State the blood parasite species.
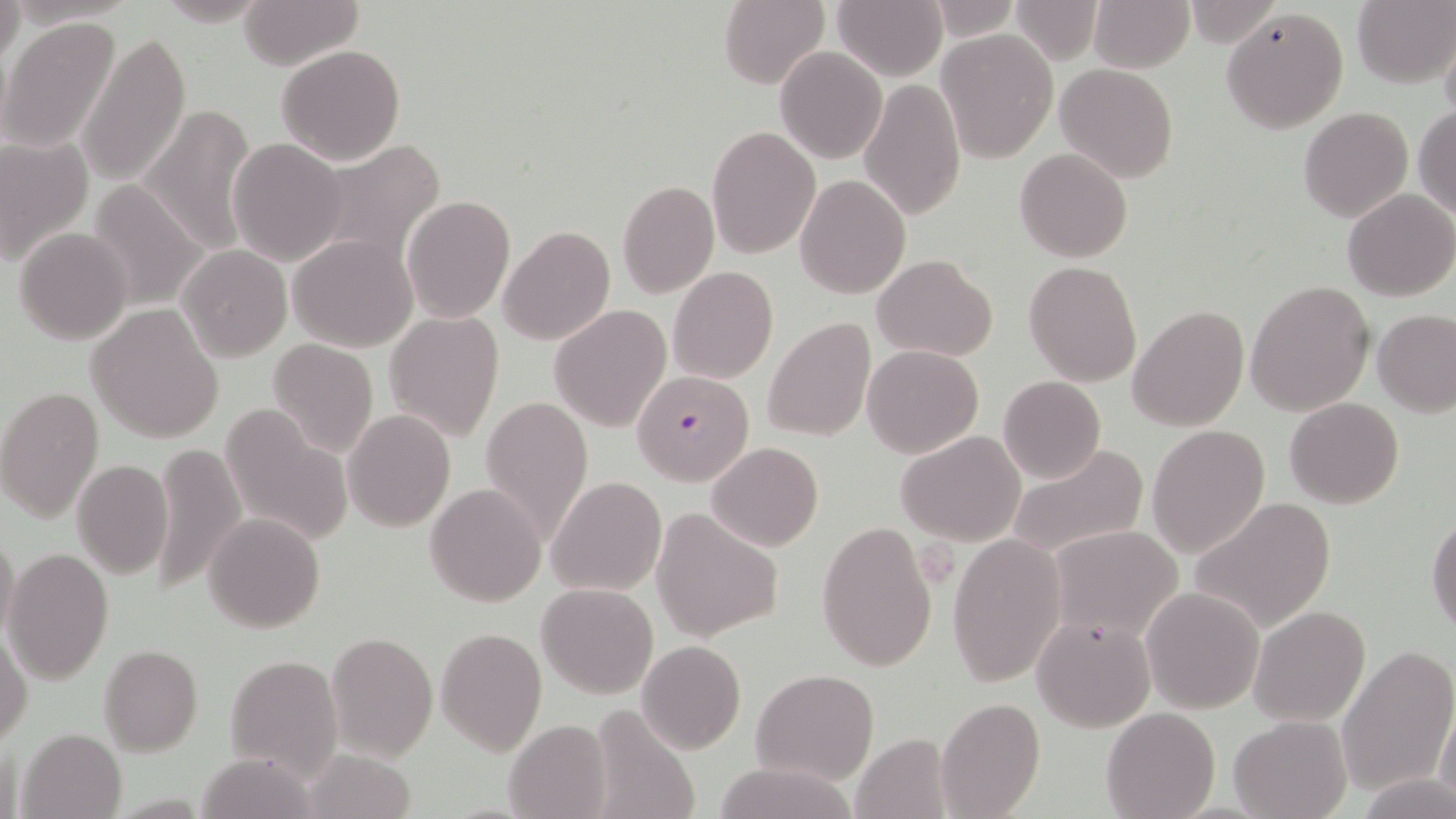

Plasmodium falciparum.

Summary:
  - Coordinate format: approximate bounding boxes as (x1,y1)-(x2,y2) corner pairs in pixels
  - Plasmodium falciparum-infected red blood cell locations: (632,369)-(755,486)
  - Uninfected red blood cell locations: (0,0)-(25,69), (150,0)-(274,27), (237,0)-(363,69), (720,0)-(830,89), (830,0)-(946,79), (1011,0)-(1104,63), (1088,0)-(1194,72), (1353,2)-(1454,87), (1220,7)-(1348,133), (2,17)-(123,154), (1441,27)-(1456,125), (937,30)-(1057,161), (79,33)-(190,186), (276,44)-(406,165), (774,47)-(886,163), (1056,63)-(1178,181), (861,76)-(966,221), (139,102)-(256,256), (1412,106)-(1456,219), (1298,107)-(1413,222), (707,126)-(820,258), (0,133)-(94,267), (227,137)-(347,266), (310,140)-(443,275), (1014,148)-(1134,263), (795,174)-(910,298), (617,179)-(719,298), (86,180)-(209,310), (1343,188)-(1456,302), (403,195)-(515,323), (498,226)-(615,346), (13,227)-(134,344), (288,235)-(419,352), (178,245)-(291,361), (873,254)-(998,361), (1024,261)-(1143,386), (668,265)-(778,383), (1245,279)-(1374,416), (86,303)-(226,443), (1128,304)-(1251,432), (550,306)-(671,431), (1373,308)-(1455,416), (384,310)-(505,442), (760,317)-(876,443), (267,338)-(379,460), (863,345)-(983,458), (998,376)-(1106,484), (0,385)-(104,524), (481,395)-(593,545), (1284,397)-(1405,508), (218,402)-(353,550), (342,408)-(455,532), (1146,424)-(1271,558), (897,430)-(1025,545), (151,441)-(247,597), (706,442)-(823,552), (1008,444)-(1148,561), (71,459)-(173,580), (547,475)-(667,596), (426,482)-(546,606), (1189,496)-(1337,634), (203,511)-(325,632), (650,511)-(783,640), (1427,513)-(1456,635), (815,520)-(938,673), (1049,524)-(1185,642), (0,527)-(20,645), (947,533)-(1066,687), (4,547)-(114,682), (537,581)-(657,699), (1140,586)-(1266,715), (1248,605)-(1373,726), (1033,615)-(1155,733), (436,626)-(547,756), (1,629)-(32,747), (325,632)-(439,762), (636,639)-(747,754), (1335,644)-(1455,797), (98,645)-(203,756), (223,653)-(342,779), (753,668)-(877,786), (937,697)-(1044,818), (1434,697)-(1455,807), (584,704)-(703,819), (1100,707)-(1220,819), (1229,715)-(1350,819), (503,719)-(612,818), (16,726)-(126,819), (851,732)-(956,819), (710,760)-(859,819), (1363,776)-(1456,818)
  - Magnification: 1000x
  - Field of view: single
  - Stain: May-Grünwald-Giemsa
  - Image size: 1456×819 pixels
  - Modality: light microscopy
  - Preparation: thin blood film